Classify this cell by malaria status.
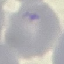

It is uninfected.

Acquired by smartphone through the microscope eyepiece. Giemsa stain. Cell patch, automatically extracted from a larger field of view and resized to 64 × 64 pixels. Thin blood smear.